Report the malaria status of this cell.
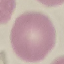
Uninfected.

Giemsa-stained preparation. Cell patch, automatically extracted from a larger field of view and resized to 64 × 64 pixels. Acquired by smartphone through the microscope eyepiece. Thin smear of blood.